Classify this cell by malaria status.
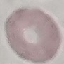
Uninfected.

{
  "capture": "smartphone through the microscope eyepiece",
  "stain": "Giemsa",
  "image_type": "cell patch, automatically extracted from a larger field of view and resized to 64 × 64 pixels",
  "preparation": "thin blood smear"
}